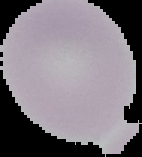

image_size: 142×157 pixels
image_type: segmented cell region on a black background
preparation: thin blood smear
malaria_status: uninfected